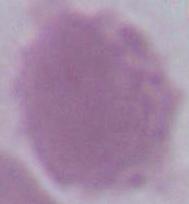
modality = micrograph
magnification = 1000x
identification = erythrocyte